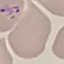

malaria status = parasitized
image type = automatically extracted cell patch, resized to 64 × 64 pixels
capture = smartphone camera at the microscope eyepiece
preparation = thin blood film
stain = Giemsa